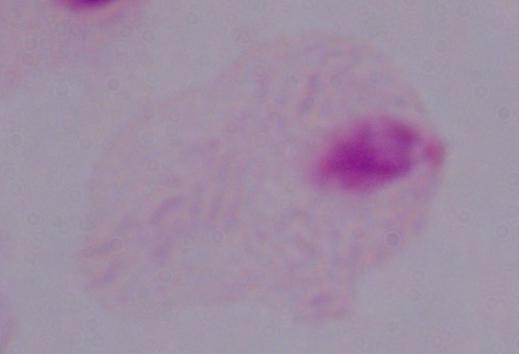
modality = photomicrograph
magnification = 1000x
identification = trichomonad